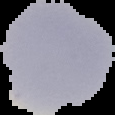

result: negative for Plasmodium parasites
image_size: 115×115 pixels
preparation: thin blood film
image_type: cell region segmented out of the field of view; surrounding area masked to black